Give the extent of all Plasmodium malariae-infected red blood cells.
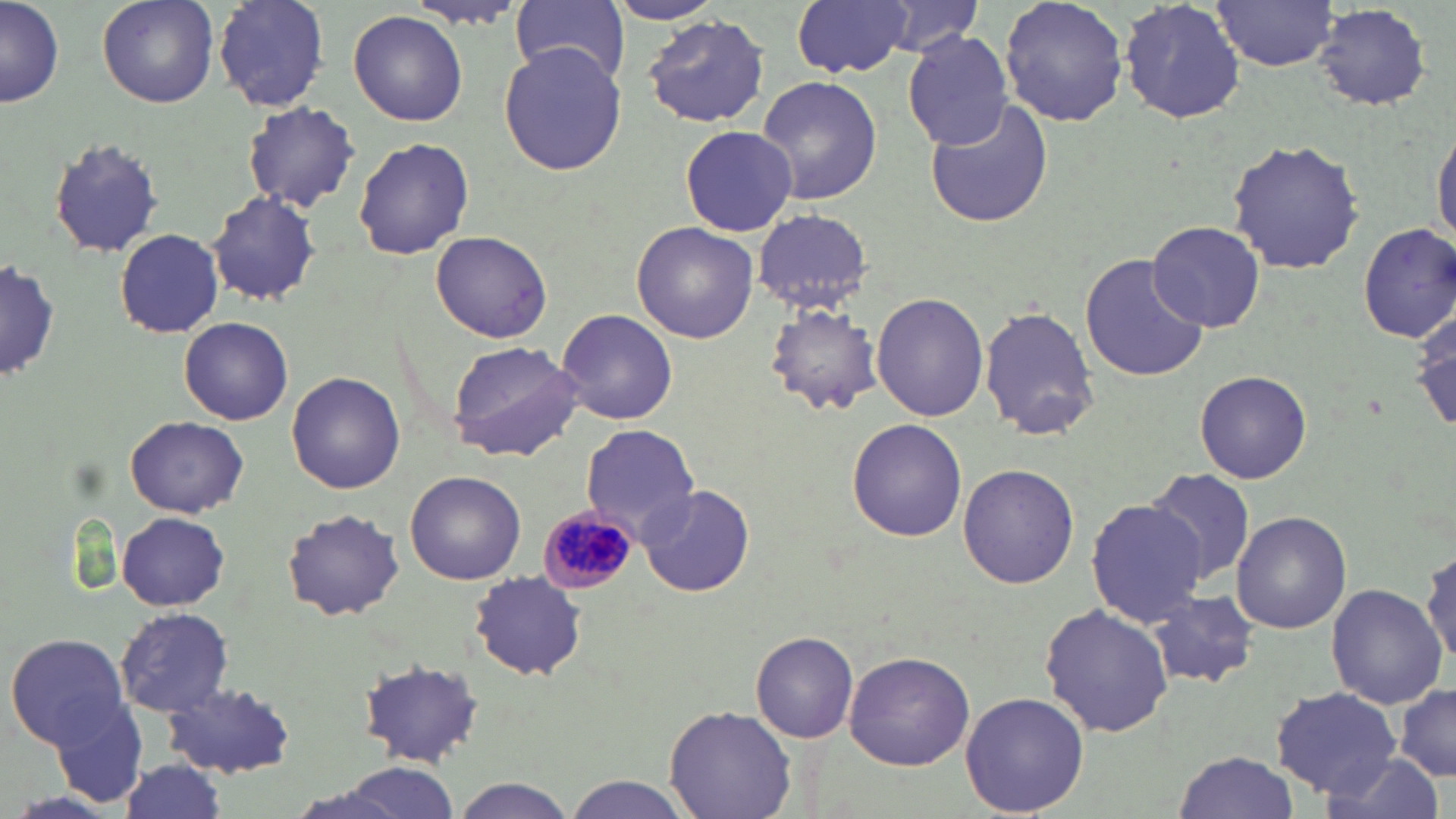

Approximate bounding boxes as (x1, y1, x2, y2) in pixels.
Plasmodium malariae-infected red blood cells: (537, 503, 636, 595).

Uninfected red blood cell locations: (95, 0, 220, 109), (211, 0, 332, 111), (397, 0, 527, 31), (791, 0, 914, 77), (866, 0, 992, 57), (998, 0, 1130, 128), (1118, 0, 1247, 126), (604, 1, 728, 26), (1214, 1, 1340, 71), (1, 2, 62, 107), (512, 2, 630, 86), (1313, 6, 1434, 111), (348, 10, 469, 127), (642, 15, 772, 129), (902, 29, 1016, 149), (498, 42, 628, 177), (758, 75, 883, 208), (925, 99, 1055, 231), (241, 102, 361, 214), (1432, 117, 1456, 252), (679, 124, 798, 237), (43, 134, 165, 258), (1227, 137, 1367, 277), (353, 138, 474, 258), (205, 190, 323, 307), (752, 208, 874, 311), (1147, 220, 1267, 332), (1355, 222, 1456, 344), (632, 223, 760, 344), (115, 228, 224, 339), (430, 230, 553, 344), (1081, 253, 1208, 383), (2, 255, 59, 386), (871, 292, 991, 423), (765, 302, 882, 415), (980, 304, 1098, 441), (1411, 304, 1456, 438), (557, 307, 678, 424), (178, 317, 294, 425), (446, 340, 585, 462), (1194, 369, 1313, 484), (287, 371, 406, 495), (125, 416, 249, 518), (846, 419, 968, 542), (581, 424, 701, 535), (957, 462, 1078, 588), (1141, 467, 1258, 585), (406, 471, 526, 584), (636, 484, 756, 598), (1085, 498, 1208, 626), (281, 508, 406, 621), (117, 510, 232, 610), (1230, 511, 1351, 634), (1420, 541, 1454, 668), (469, 574, 586, 680), (1327, 584, 1446, 709), (1146, 589, 1261, 690), (1039, 603, 1174, 739), (114, 607, 234, 716), (751, 631, 859, 744), (5, 632, 129, 749), (843, 650, 974, 770), (357, 659, 485, 768), (164, 682, 300, 779), (1396, 682, 1456, 780), (1271, 688, 1401, 795), (42, 691, 152, 812), (960, 691, 1090, 815), (665, 705, 796, 819), (1170, 749, 1297, 819), (1319, 754, 1441, 819), (111, 760, 230, 819), (317, 764, 467, 819), (565, 777, 694, 819), (451, 778, 580, 818). Slide-level diagnosis: Plasmodium malariae. Thin blood film. Image is 1456×819 pixels. One field of a larger specimen. 1000x magnification. Optical microscopy. May-Grünwald-Giemsa-stained preparation.